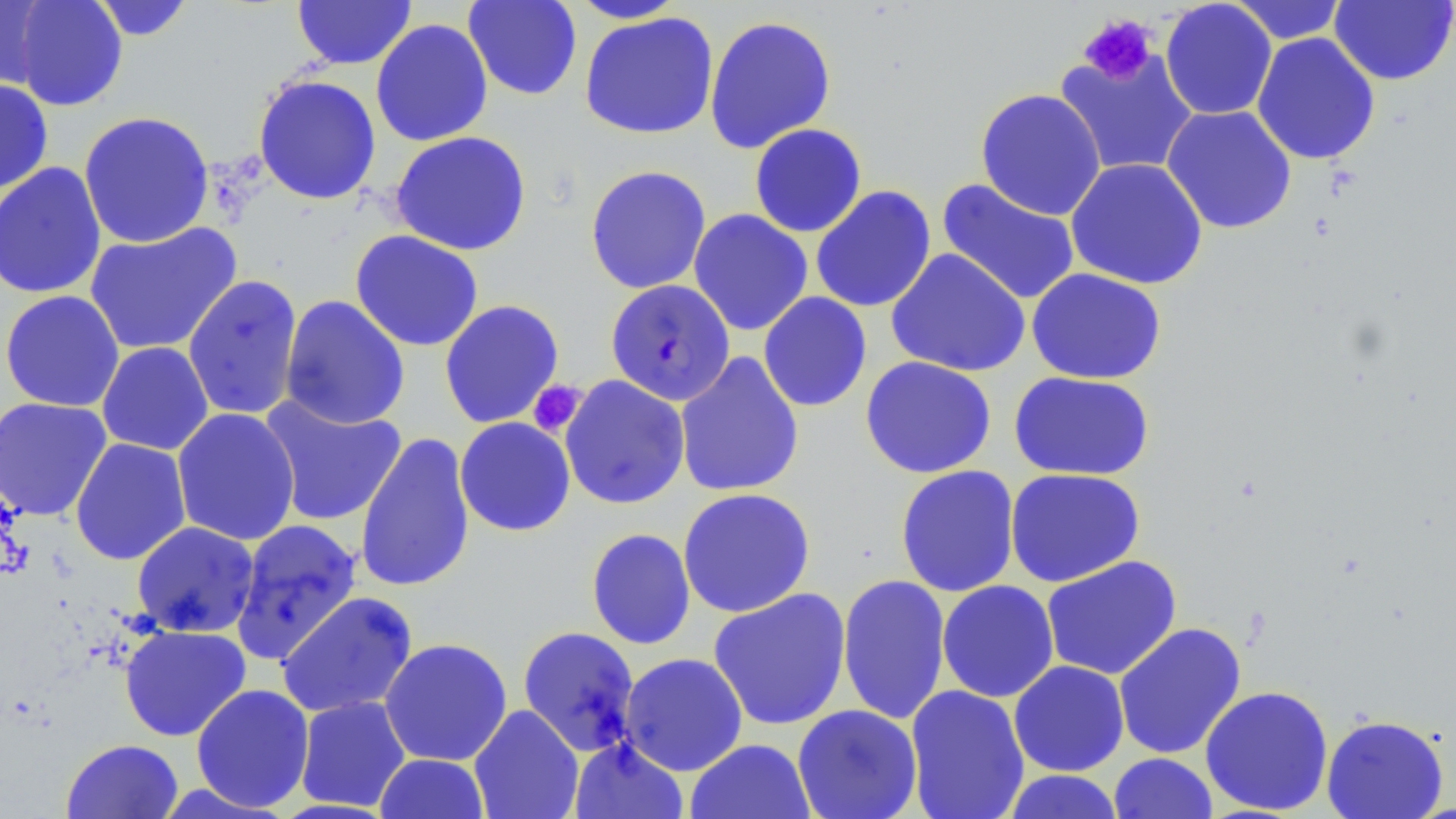
{
  "slide_level_diagnosis": "Plasmodium falciparum",
  "image_size": "1456×819 pixels",
  "preparation": "thin blood smear",
  "stain": "May-Grünwald-Giemsa",
  "plasmodium_falciparum_infected_red_blood_cell_locations": "approximate bounding boxes as (x1,y1)-(x2,y2) corner pairs in pixels: (605,279)-(735,406)",
  "modality": "optical microscopy",
  "magnification": "1000x",
  "platelet_locations": "approximate bounding boxes as (x1,y1)-(x2,y2) corner pairs in pixels: (1078,13)-(1157,85), (528,380)-(587,437)",
  "uninfected_red_blood_cell_locations": "approximate bounding boxes as (x1,y1)-(x2,y2) corner pairs in pixels: (0,0)-(52,90), (11,0)-(128,111), (89,0)-(196,41), (292,0)-(417,69), (463,0)-(582,101), (566,0)-(689,23), (1227,0)-(1350,44), (1329,0)-(1455,86), (1160,1)-(1277,120), (579,11)-(719,140), (704,14)-(837,154), (370,19)-(493,147), (1251,32)-(1381,166), (1053,49)-(1199,178), (253,74)-(381,205), (0,78)-(54,195), (975,88)-(1106,220), (1161,105)-(1297,235), (78,110)-(215,249), (748,123)-(867,238), (390,130)-(532,256), (1065,157)-(1208,290), (0,162)-(107,300), (585,164)-(712,294), (936,178)-(1080,306), (810,185)-(936,313), (688,209)-(814,336), (84,222)-(243,356), (350,230)-(484,352), (886,248)-(1031,378), (1026,267)-(1167,384), (182,274)-(303,421), (1,290)-(125,412), (758,292)-(872,412), (279,295)-(410,430), (439,300)-(565,428), (97,341)-(214,456), (674,351)-(805,498), (860,356)-(997,479), (1009,371)-(1155,480), (559,375)-(691,510), (258,394)-(407,527), (0,397)-(113,521), (171,408)-(301,546), (454,417)-(576,537), (355,431)-(476,594), (70,437)-(192,566), (895,464)-(1021,598), (1004,467)-(1146,588), (677,487)-(816,618), (230,519)-(363,666), (131,521)-(260,638), (586,528)-(696,650), (1041,555)-(1183,680), (836,573)-(952,726), (936,580)-(1059,703), (708,588)-(852,730), (276,591)-(418,718), (1113,621)-(1247,760), (119,624)-(251,742), (517,626)-(641,756), (379,637)-(513,766), (619,652)-(748,775), (1008,660)-(1129,777), (191,684)-(315,813), (904,684)-(1030,819), (1199,685)-(1334,816), (294,695)-(411,812), (468,704)-(584,819), (792,704)-(923,819), (1321,713)-(1449,819), (570,737)-(688,819), (61,739)-(183,819), (685,739)-(816,819), (1108,752)-(1218,819), (374,753)-(490,818), (1001,769)-(1125,819)",
  "field_of_view": "single"
}